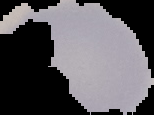

preparation: thin blood film
malaria_status: uninfected
image_type: segmented cell region with the area outside set to black
image_size: 154×115 pixels